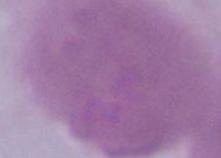 Micrograph. Captured at 1000x magnification. A red blood cell is seen.